Locate and identify every blood parasite.
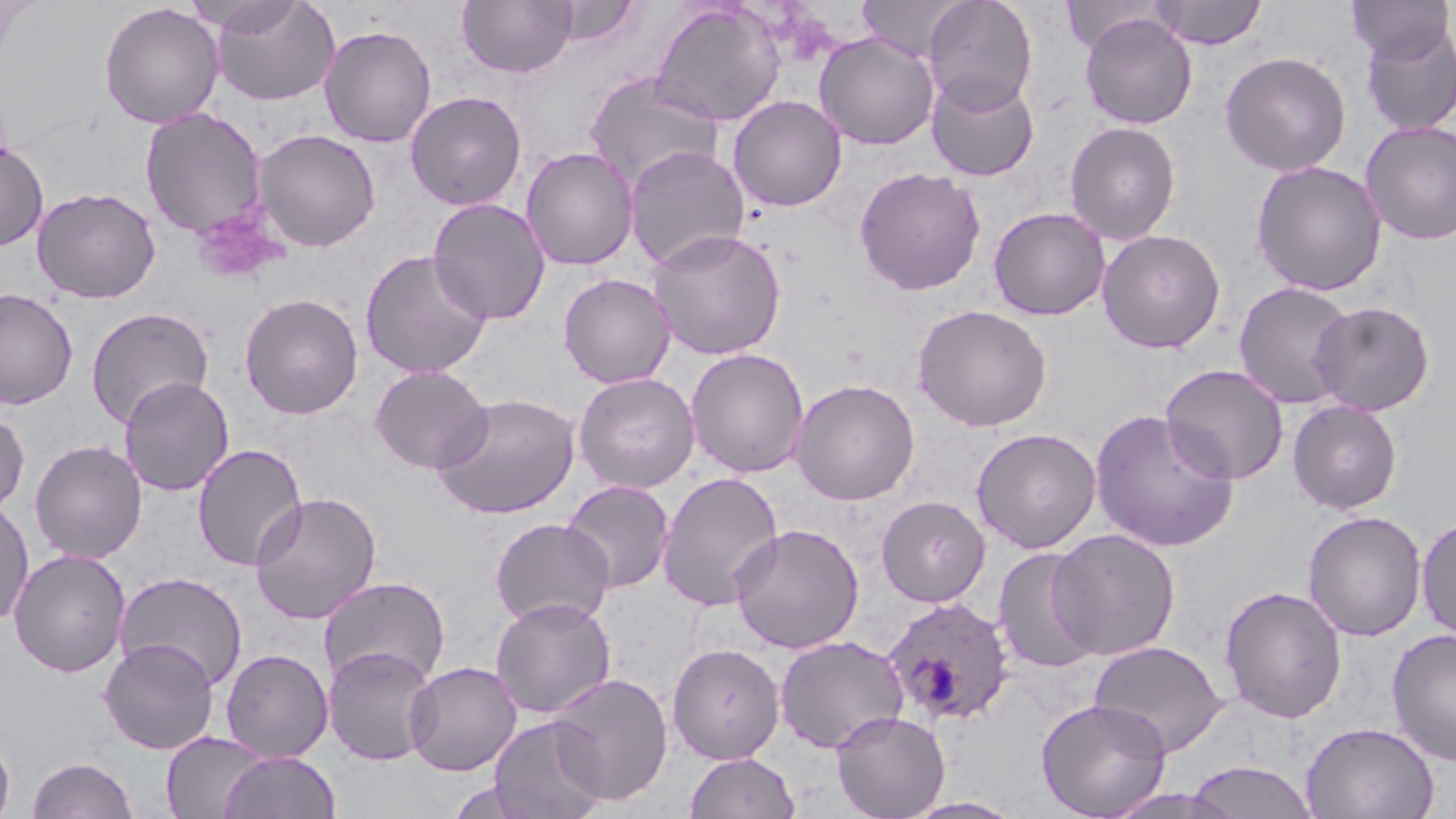
Approximate bounding boxes as (x1, y1, x2, y2) in pixels.
Plasmodium ovale-infected red blood cells: (882, 597, 1016, 726).
No Plasmodium falciparum, Plasmodium malariae, Plasmodium vivax, Babesia divergens, or Trypanosoma brucei observed.

Platelet locations: (191, 208, 284, 285). Uninfected red blood cell locations: (208, 0, 340, 106), (457, 0, 578, 78), (857, 0, 973, 63), (923, 0, 1038, 113), (1148, 0, 1267, 49), (1347, 0, 1453, 65), (99, 2, 225, 128), (547, 2, 640, 47), (649, 2, 787, 127), (1079, 13, 1197, 129), (319, 24, 437, 147), (1361, 27, 1456, 136), (814, 32, 940, 150), (1220, 51, 1351, 176), (926, 73, 1040, 182), (584, 75, 723, 191), (405, 91, 527, 211), (728, 95, 847, 212), (139, 107, 267, 239), (1359, 120, 1456, 245), (1064, 121, 1181, 245), (253, 129, 381, 252), (0, 139, 49, 252), (623, 145, 751, 272), (521, 147, 638, 270), (1251, 160, 1388, 296), (854, 167, 986, 295), (31, 187, 160, 303), (428, 197, 551, 325), (989, 206, 1110, 320), (645, 227, 786, 361), (1096, 228, 1226, 354), (359, 249, 492, 379), (558, 273, 676, 388), (1233, 281, 1358, 410), (0, 288, 79, 409), (239, 293, 364, 419), (1310, 301, 1436, 416), (913, 304, 1052, 432), (85, 306, 215, 429), (686, 347, 809, 478), (1160, 364, 1289, 485), (369, 365, 492, 474), (573, 371, 700, 493), (118, 376, 234, 497), (789, 378, 920, 506), (431, 392, 581, 520), (1287, 399, 1403, 514), (0, 408, 29, 519), (1090, 408, 1240, 552), (971, 427, 1102, 554), (29, 439, 147, 563), (192, 444, 308, 571), (657, 471, 785, 612), (561, 480, 674, 593), (249, 491, 384, 625), (875, 494, 990, 607), (0, 498, 34, 628), (1302, 510, 1427, 642), (1416, 515, 1456, 643), (489, 517, 615, 630), (730, 524, 864, 654), (1046, 528, 1181, 661), (992, 547, 1105, 674), (8, 548, 132, 677), (114, 571, 248, 692), (318, 576, 450, 689), (1219, 585, 1348, 723), (490, 596, 616, 719), (1386, 628, 1456, 767), (774, 635, 909, 754), (98, 638, 219, 754), (1088, 640, 1228, 758), (667, 642, 786, 763), (322, 644, 439, 766), (220, 649, 333, 762), (404, 661, 522, 776), (547, 673, 674, 805), (1036, 698, 1172, 818), (830, 710, 950, 819), (487, 715, 609, 819), (1303, 722, 1440, 819), (161, 732, 269, 819), (0, 733, 15, 819), (217, 751, 341, 819), (684, 751, 801, 819), (27, 756, 138, 819), (1183, 761, 1319, 819), (1100, 787, 1240, 819), (900, 796, 1027, 819). Slide-level diagnosis: Plasmodium ovale. Captured at 1000x magnification. Image is 1456×819 pixels. May-Grünwald-Giemsa-stained preparation. Light microscopy. Single field of view. Thin blood smear.